Locate every Plasmodium falciparum-infected red blood cell.
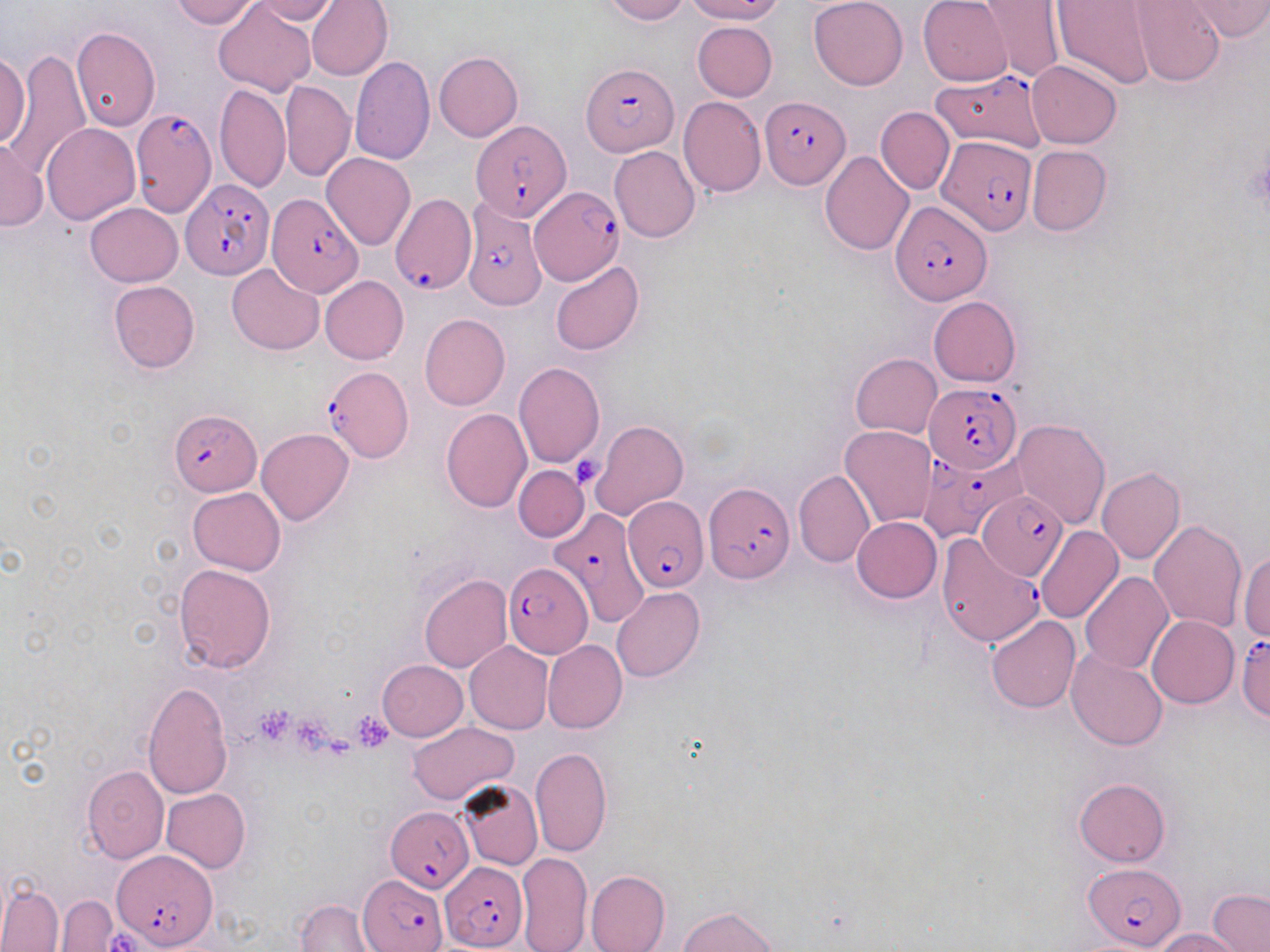

Approximate bounding boxes as (x1, y1, x2, y2) in pixels.
Plasmodium falciparum-infected red blood cells: (581, 61, 676, 156), (931, 71, 1047, 152), (760, 96, 851, 189), (132, 108, 217, 216), (472, 121, 570, 220), (935, 134, 1038, 235), (183, 180, 272, 279), (530, 187, 625, 284), (266, 193, 363, 297), (390, 194, 474, 296), (462, 198, 548, 311), (891, 200, 992, 304), (323, 366, 412, 462), (924, 381, 1021, 474), (170, 410, 262, 496), (915, 452, 1005, 545), (704, 480, 793, 583), (978, 491, 1067, 580), (626, 496, 707, 593), (544, 508, 650, 623), (938, 534, 1045, 647), (504, 562, 591, 658), (1236, 634, 1270, 723), (386, 806, 474, 892), (114, 850, 218, 949), (441, 862, 526, 950), (1083, 863, 1187, 949), (360, 875, 448, 949).

Summary:
  - Uninfected red blood cell locations: (169, 0, 262, 28), (249, 0, 339, 24), (306, 0, 393, 81), (599, 0, 688, 24), (686, 0, 785, 23), (809, 0, 907, 89), (918, 0, 1012, 86), (979, 0, 1066, 84), (1052, 1, 1156, 88), (1130, 1, 1225, 86), (1182, 1, 1270, 40), (212, 2, 317, 97), (692, 21, 777, 100), (71, 25, 160, 132), (0, 48, 91, 181), (0, 51, 31, 148), (434, 51, 523, 142), (349, 56, 435, 164), (1027, 61, 1121, 148), (281, 80, 354, 180), (214, 84, 289, 192), (678, 97, 766, 197), (876, 107, 954, 194), (42, 121, 140, 224), (0, 138, 46, 232), (1026, 145, 1111, 236), (610, 146, 700, 241), (819, 150, 914, 255), (322, 152, 416, 250), (85, 203, 182, 286), (550, 260, 644, 356), (227, 264, 324, 355), (320, 275, 408, 364), (108, 280, 200, 373), (928, 296, 1021, 387), (419, 314, 510, 411), (850, 353, 941, 438), (513, 362, 605, 469), (441, 409, 531, 513), (1011, 419, 1110, 529), (590, 420, 688, 519), (839, 426, 938, 529), (256, 429, 354, 525), (513, 465, 588, 542), (1096, 467, 1185, 565), (794, 470, 874, 568), (1112, 478, 1213, 601), (187, 487, 285, 576), (852, 516, 941, 602), (1148, 520, 1247, 632), (1034, 526, 1123, 624), (1090, 547, 1239, 662), (1239, 552, 1270, 640), (173, 564, 276, 672), (1079, 572, 1174, 673), (419, 573, 512, 673), (611, 587, 704, 682), (1147, 615, 1240, 709), (986, 616, 1080, 713), (543, 639, 626, 733), (465, 641, 554, 734), (1067, 649, 1169, 752), (377, 660, 468, 741), (142, 681, 233, 799), (407, 721, 519, 803), (530, 746, 612, 857), (82, 764, 170, 863), (1074, 777, 1171, 867), (458, 780, 543, 871), (161, 788, 251, 873), (517, 852, 593, 952), (585, 869, 671, 952), (0, 880, 63, 952), (1207, 887, 1270, 952), (56, 895, 118, 951), (295, 899, 375, 951), (679, 905, 779, 952), (1151, 928, 1247, 951)
  - Platelet locations: (1249, 151, 1270, 211), (571, 456, 605, 488), (254, 705, 294, 743), (355, 712, 391, 751), (294, 716, 330, 748), (108, 931, 139, 950)
  - Slide-level diagnosis: Plasmodium falciparum
  - Magnification: 1000x
  - Image size: 1270×952 pixels
  - Preparation: thin blood film
  - Stain: May-Grünwald-Giemsa
  - Modality: optical microscopy
  - Field of view: one of a larger specimen